Report the malaria status of this cell.
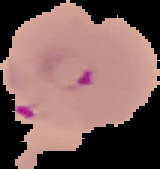

It is parasitized.

Image is 160×169 pixels. From a thin blood film. The area outside the segmented cell region is set to black.